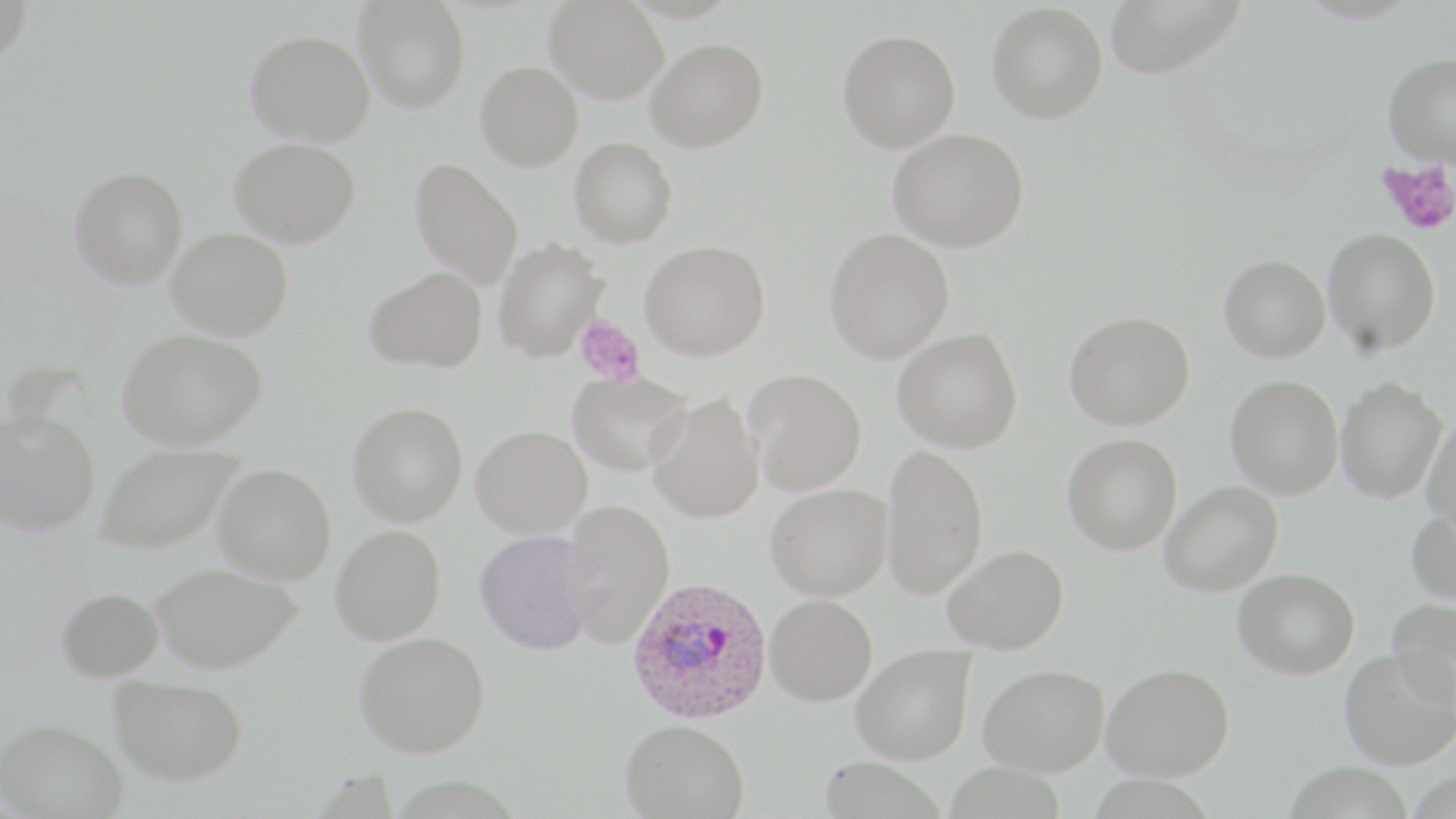
plasmodium_ovale_infected_red_blood_cell_locations: 'approximate bounding boxes as (x1, y1, x2, y2) in pixels: (628, 577, 773, 724)'
slide_level_diagnosis: Plasmodium ovale
modality: light microscopy
platelet_locations: 'approximate bounding boxes as (x1, y1, x2, y2) in pixels: (1378, 159, 1456, 235), (575, 317, 645, 386)'
uninfected_red_blood_cell_locations: 'approximate bounding boxes as (x1, y1, x2, y2) in pixels: (0, 0, 34, 68), (354, 0, 470, 113), (544, 0, 669, 103), (1103, 0, 1244, 78), (986, 2, 1108, 123), (837, 28, 961, 153), (245, 29, 375, 146), (645, 38, 769, 152), (1382, 52, 1456, 166), (475, 60, 583, 171), (888, 128, 1029, 252), (230, 137, 361, 246), (569, 137, 679, 247), (409, 158, 524, 289), (69, 166, 187, 288), (166, 228, 293, 341), (824, 228, 954, 363), (1322, 228, 1442, 354), (494, 238, 610, 361), (640, 240, 770, 361), (1218, 254, 1330, 362), (364, 266, 487, 373), (1064, 310, 1195, 430), (893, 327, 1023, 453), (118, 328, 267, 449), (744, 368, 866, 495), (567, 371, 690, 476), (1225, 375, 1343, 498), (1335, 377, 1447, 503), (646, 392, 764, 523), (347, 402, 468, 526), (0, 408, 101, 535), (1421, 417, 1456, 536), (472, 425, 592, 538), (1062, 433, 1182, 555), (94, 442, 244, 554), (881, 444, 988, 599), (212, 463, 336, 584), (1159, 481, 1283, 596), (765, 483, 892, 600), (564, 498, 675, 649), (1406, 507, 1456, 607), (329, 524, 445, 644), (475, 530, 594, 655), (941, 544, 1069, 654), (151, 563, 301, 672), (1233, 568, 1360, 679), (55, 586, 164, 681), (765, 594, 877, 706), (1387, 598, 1456, 710), (355, 631, 490, 756), (850, 645, 975, 764), (1338, 647, 1456, 770), (1102, 662, 1234, 780), (979, 663, 1109, 775), (109, 675, 247, 784), (1, 718, 128, 818), (620, 718, 748, 818), (818, 756, 946, 818)'
image_size: 1456×819 pixels
preparation: thin blood film
field_of_view: one of a larger specimen
stain: May-Grünwald-Giemsa
magnification: 1000x